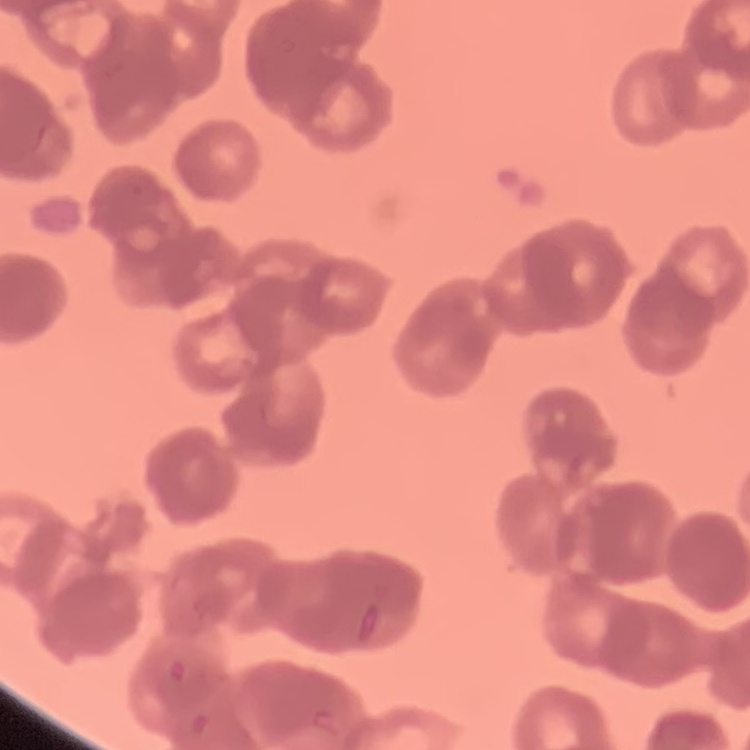
Summary:
  - Erythrocyte morphology: rouleaux formation
  - Image type: one tile cut from a larger photomicrograph
  - Preparation: thin blood smear
  - Stain: Field's or Giemsa